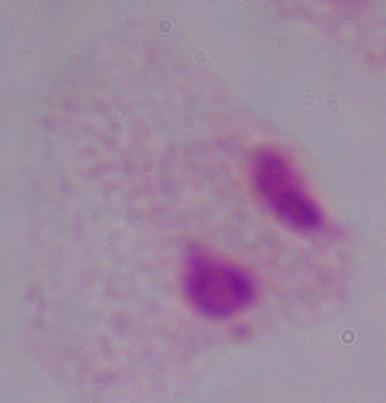

1000x magnification. A trichomonad is shown. Micrograph.